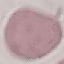
{
  "malaria_status": "uninfected",
  "preparation": "thin blood film",
  "image_type": "cell patch, automatically extracted from a larger field of view and resized to 64 × 64 pixels",
  "capture": "smartphone camera at the microscope eyepiece",
  "stain": "Giemsa"
}